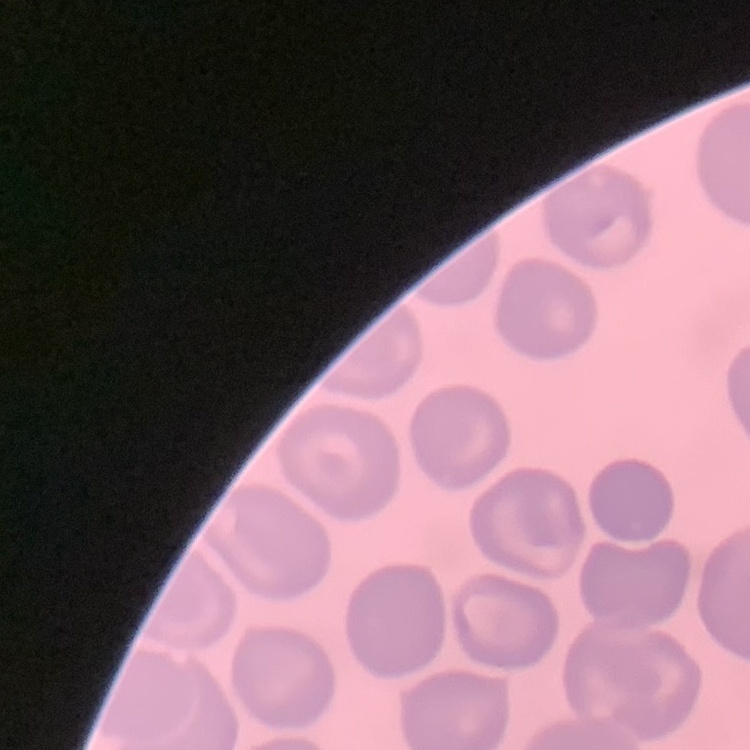
Summary:
  - Erythrocyte morphology: no rouleaux formation
  - Stain: Field's or Giemsa
  - Preparation: thin blood smear
  - Image type: one tile cut from a larger photomicrograph